Report the malaria status of this cell.
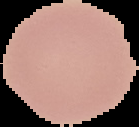

Uninfected.

{
  "image_type": "segmented cell region with the area outside set to black",
  "preparation": "thin blood smear",
  "image_size": "139×127 pixels"
}